Give the position of every Plasmodium parasite visible.
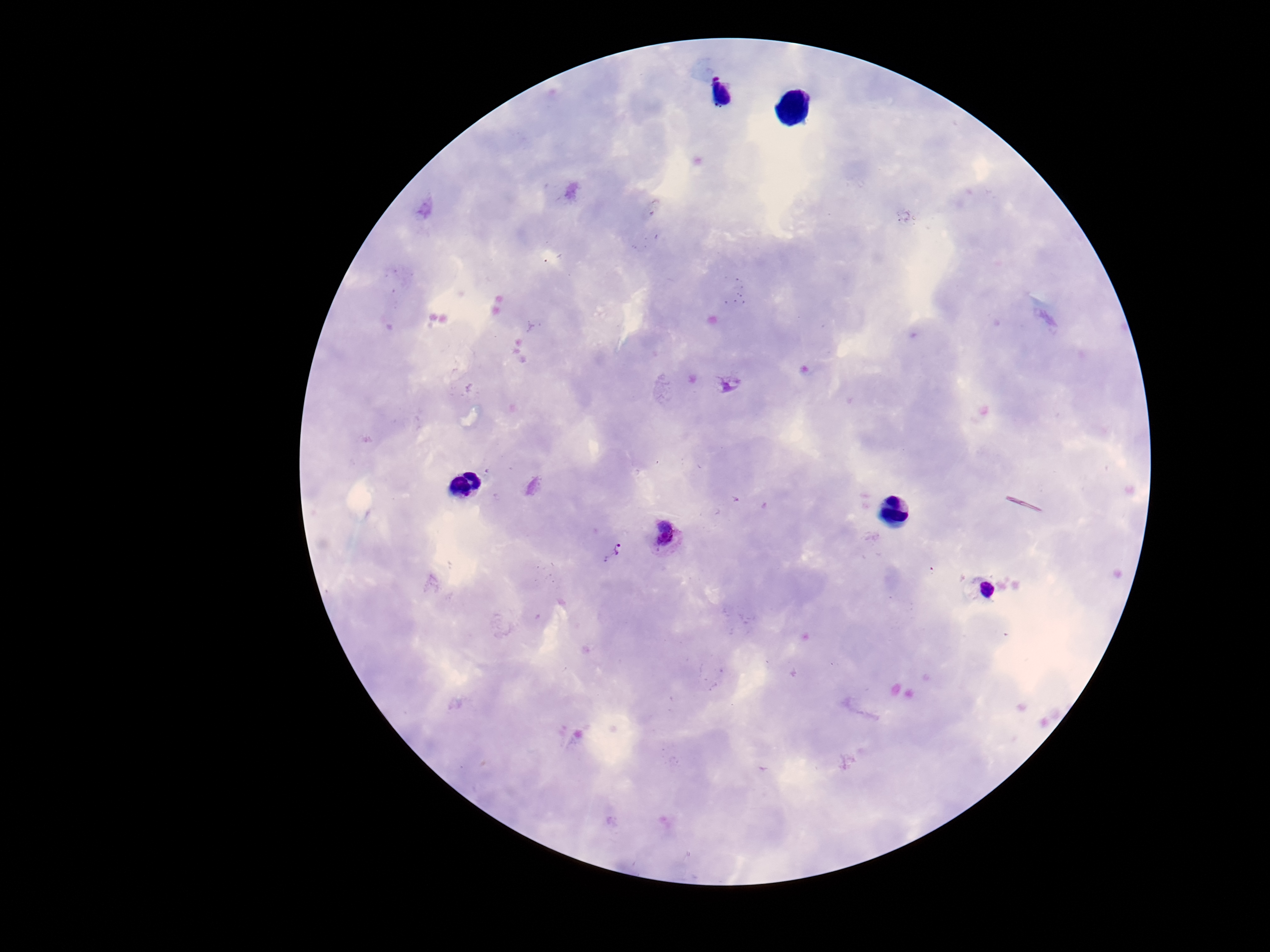
Approximate object centers, in pixels from the top-left corner.
Plasmodium parasites: (x=667, y=534), (x=612, y=550).

Summary:
  - Image size: 1270×952 pixels
  - Field of view: one from this slide
  - Preparation: thick blood film
  - Stain: Giemsa
  - Capture: smartphone camera through the microscope eyepiece
  - Magnification: 100x
  - Patient malaria status: positive